State the blood parasite species.
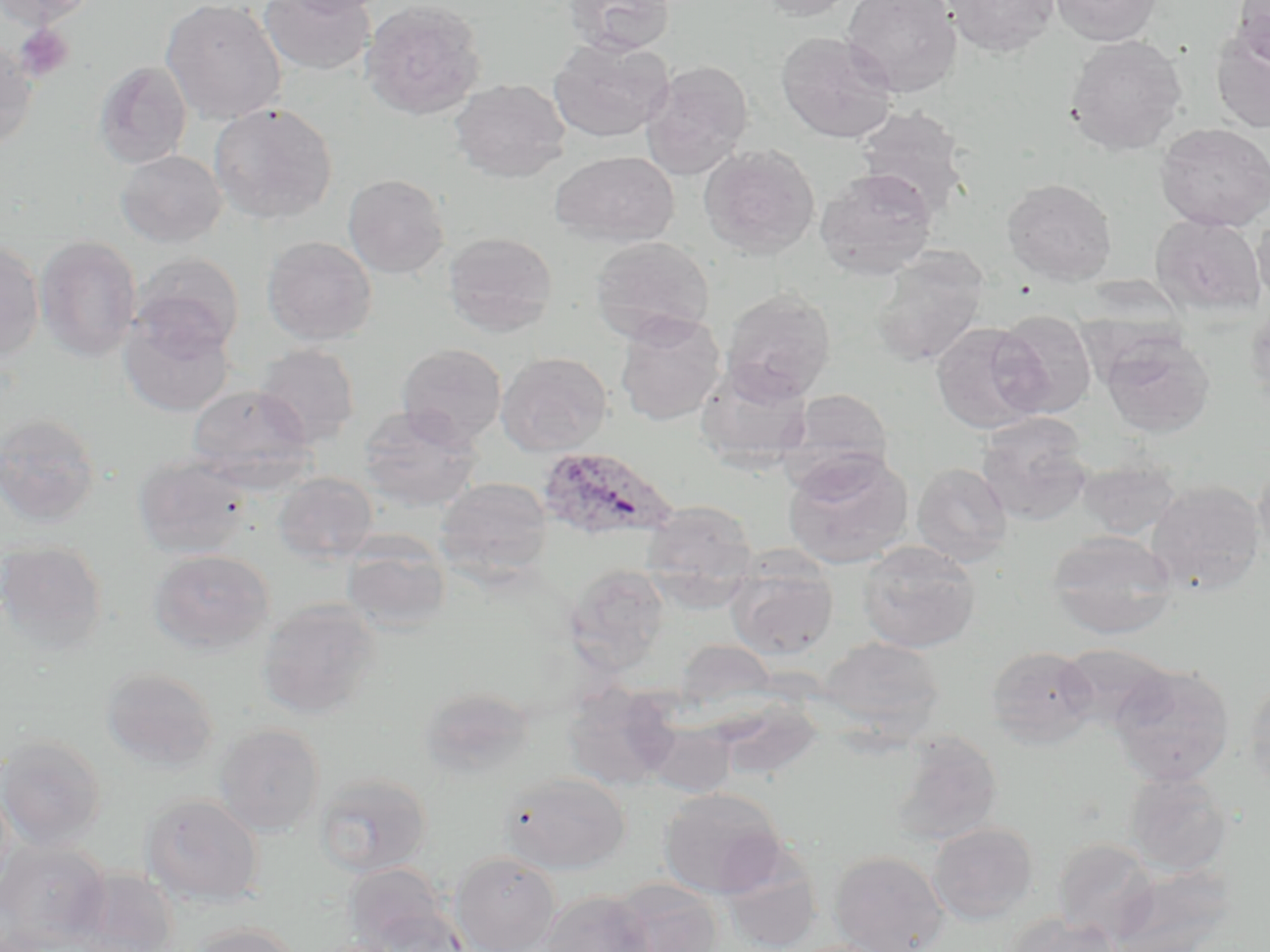

Plasmodium ovale.

magnification = 1000x
Plasmodium ovale-infected red blood cell locations = approximate bounding boxes as (x1, y1, x2, y2) in pixels: (537, 445, 678, 543)
image size = 1270×952 pixels
platelet locations = approximate bounding boxes as (x1, y1, x2, y2) in pixels: (14, 24, 75, 83)
uninfected red blood cell locations = approximate bounding boxes as (x1, y1, x2, y2) in pixels: (0, 0, 100, 28), (160, 0, 286, 124), (276, 0, 388, 16), (360, 0, 487, 121), (565, 0, 677, 55), (754, 0, 861, 21), (841, 0, 962, 98), (942, 0, 1060, 57), (1049, 0, 1162, 46), (1233, 0, 1270, 66), (258, 1, 375, 76), (1053, 12, 1178, 103), (1210, 28, 1270, 134), (776, 30, 898, 144), (1065, 35, 1188, 156), (549, 37, 674, 142), (0, 40, 38, 152), (94, 60, 192, 168), (641, 60, 754, 178), (449, 78, 571, 182), (208, 101, 338, 225), (853, 105, 972, 217), (1154, 122, 1270, 231), (699, 144, 820, 258), (116, 150, 227, 248), (550, 151, 679, 247), (815, 167, 938, 279), (342, 173, 450, 279), (1001, 178, 1118, 285), (1251, 212, 1270, 312), (1150, 213, 1266, 316), (443, 231, 558, 337), (35, 235, 141, 362), (262, 235, 378, 345), (589, 236, 715, 343), (0, 241, 45, 363), (871, 248, 990, 368), (130, 253, 244, 356), (721, 287, 837, 402), (1245, 300, 1270, 408), (990, 309, 1098, 418), (118, 310, 236, 417), (614, 312, 726, 426), (931, 322, 1049, 433), (1100, 330, 1215, 438), (397, 343, 507, 447), (254, 344, 360, 447), (496, 352, 613, 456), (695, 362, 814, 472), (187, 384, 315, 486), (780, 387, 895, 490), (357, 406, 481, 511), (0, 413, 102, 528), (976, 413, 1094, 527), (783, 450, 914, 569), (133, 453, 253, 560), (1077, 457, 1182, 540), (1253, 459, 1270, 569), (912, 462, 1013, 566), (273, 471, 378, 564), (435, 477, 553, 584), (1146, 480, 1266, 597), (641, 500, 758, 596), (1046, 529, 1179, 639), (340, 535, 452, 634), (0, 540, 109, 653), (857, 541, 980, 653), (148, 548, 274, 655), (726, 555, 838, 660), (564, 563, 671, 673), (257, 598, 382, 718), (818, 636, 945, 736), (675, 639, 779, 709), (1057, 643, 1174, 732), (986, 644, 1098, 748), (1110, 663, 1235, 786), (101, 666, 220, 772), (1243, 677, 1270, 792), (561, 683, 680, 791), (420, 686, 536, 781), (643, 721, 736, 797), (213, 723, 325, 836), (890, 731, 1004, 847), (0, 735, 107, 850), (1124, 771, 1234, 875), (314, 772, 433, 877), (500, 772, 630, 874), (659, 787, 789, 898), (141, 793, 264, 908), (928, 822, 1038, 924), (1052, 838, 1161, 944), (0, 840, 110, 951), (829, 850, 950, 952), (450, 851, 561, 952), (719, 851, 823, 952), (343, 862, 455, 951), (1108, 862, 1236, 952), (67, 867, 180, 952), (609, 879, 724, 952), (540, 890, 655, 952), (364, 905, 470, 951), (1001, 914, 1125, 952), (189, 922, 302, 952), (308, 938, 402, 952)
modality = optical microscopy
preparation = thin blood film
stain = May-Grünwald-Giemsa
field of view = one of a larger specimen